Report the malaria status of this cell.
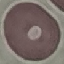
Uninfected.

Photographed with a smartphone camera at the microscope eyepiece. Thin blood smear. Giemsa-stained preparation. Automatically extracted cell patch, resized to 64 × 64 pixels.